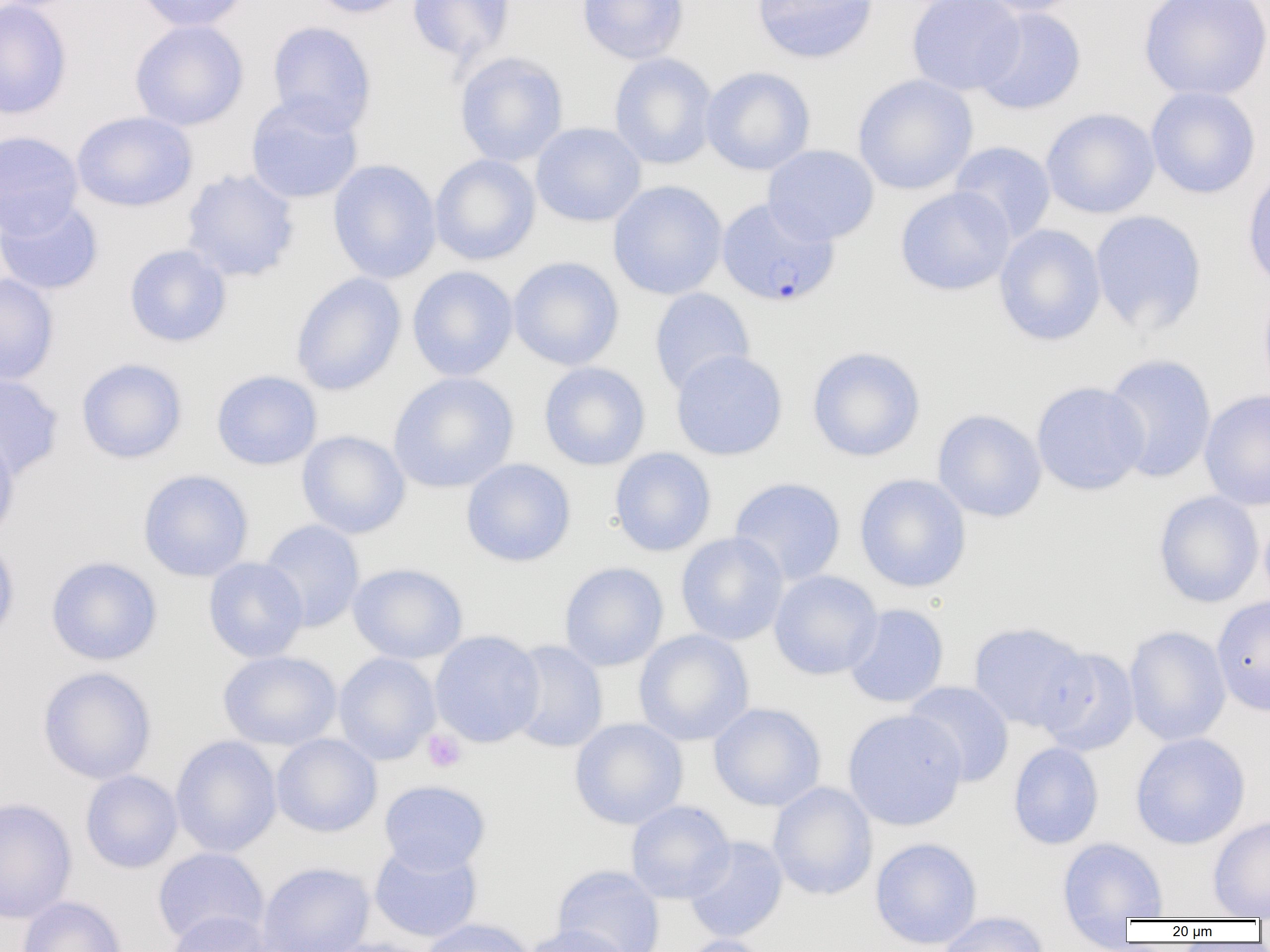
Summary:
  - Coordinate format: approximate bounding boxes as (x1, y1, x2, y2) in pixels
  - Plasmodium falciparum-infected red blood cell locations: (716, 197, 839, 307)
  - Platelet locations: (422, 729, 467, 773)
  - Uninfected red blood cell locations: (0, 0, 72, 120), (134, 0, 251, 32), (304, 0, 416, 19), (406, 0, 516, 65), (577, 0, 689, 64), (750, 0, 878, 64), (906, 0, 1025, 95), (971, 0, 1085, 16), (1139, 0, 1270, 101), (973, 6, 1086, 115), (129, 20, 249, 131), (266, 21, 377, 134), (453, 51, 569, 167), (608, 52, 718, 170), (701, 66, 816, 175), (852, 74, 978, 195), (1146, 85, 1261, 199), (245, 95, 364, 204), (1040, 108, 1160, 218), (71, 111, 198, 212), (531, 122, 646, 227), (0, 131, 84, 238), (949, 141, 1056, 243), (763, 145, 879, 245), (430, 154, 541, 265), (327, 159, 441, 284), (1242, 164, 1270, 292), (180, 169, 301, 282), (607, 180, 728, 300), (895, 186, 1015, 296), (0, 197, 104, 296), (1089, 210, 1207, 335), (993, 224, 1106, 346), (123, 244, 232, 348), (508, 256, 624, 370), (407, 266, 519, 381), (290, 272, 406, 396), (0, 273, 59, 385), (1258, 281, 1270, 401), (649, 288, 755, 395), (806, 346, 926, 462), (670, 349, 788, 461), (1102, 353, 1217, 483), (76, 358, 189, 464), (539, 362, 651, 470), (211, 369, 322, 470), (388, 371, 519, 493), (0, 373, 64, 479), (1031, 381, 1150, 495), (1199, 389, 1270, 511), (932, 409, 1047, 522), (0, 430, 20, 544), (296, 430, 410, 539), (609, 447, 717, 557), (461, 458, 576, 567), (137, 469, 254, 582), (854, 473, 972, 593), (728, 477, 847, 586), (1153, 491, 1264, 608), (1259, 510, 1270, 612), (258, 519, 365, 632), (675, 531, 789, 646), (0, 537, 20, 645), (45, 556, 163, 665), (203, 557, 309, 662), (348, 562, 468, 664), (558, 562, 669, 671), (769, 570, 883, 680), (1211, 595, 1270, 716), (844, 603, 950, 708), (968, 622, 1091, 732), (1124, 625, 1231, 746), (633, 629, 754, 746), (429, 630, 545, 747), (506, 640, 608, 753), (1036, 647, 1140, 756), (218, 650, 342, 751), (333, 652, 440, 765), (37, 666, 157, 784), (903, 681, 1015, 786), (708, 702, 826, 811), (842, 709, 968, 830), (569, 718, 688, 829), (271, 733, 382, 837), (1129, 733, 1250, 850), (170, 735, 282, 857), (1007, 742, 1104, 849), (80, 770, 183, 874), (378, 779, 491, 874), (768, 782, 878, 901), (0, 797, 77, 923), (625, 800, 735, 903), (1208, 815, 1270, 919), (684, 836, 788, 943), (870, 837, 983, 949), (1057, 837, 1168, 919), (368, 841, 483, 942), (152, 847, 268, 946), (256, 861, 375, 952), (552, 865, 665, 952), (17, 896, 126, 952), (162, 911, 275, 952), (937, 911, 1050, 952), (418, 918, 535, 952), (522, 924, 633, 952), (674, 934, 774, 952), (316, 938, 437, 952)
  - Slide-level diagnosis: Plasmodium falciparum
  - Magnification: 1000x
  - Modality: optical microscopy
  - Image size: 1270×952 pixels
  - Field of view: single
  - Preparation: thin blood smear